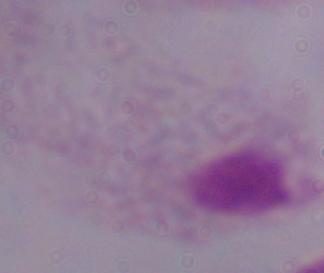
Summary:
  - Modality: micrograph
  - Magnification: 1000x
  - Identification: trichomonad